Report the malaria status of this cell.
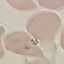
Uninfected.

preparation = thin blood film
image type = cell patch, automatically extracted from a larger field of view and resized to 64 × 64 pixels
capture = smartphone through the microscope eyepiece
stain = Giemsa